Report the malaria status of this cell.
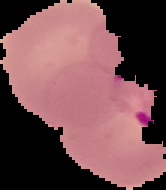

It is parasitized.

From a thin blood smear. Cell region segmented out of the field of view; the surrounding area is masked to black. Image is 166×190 pixels.